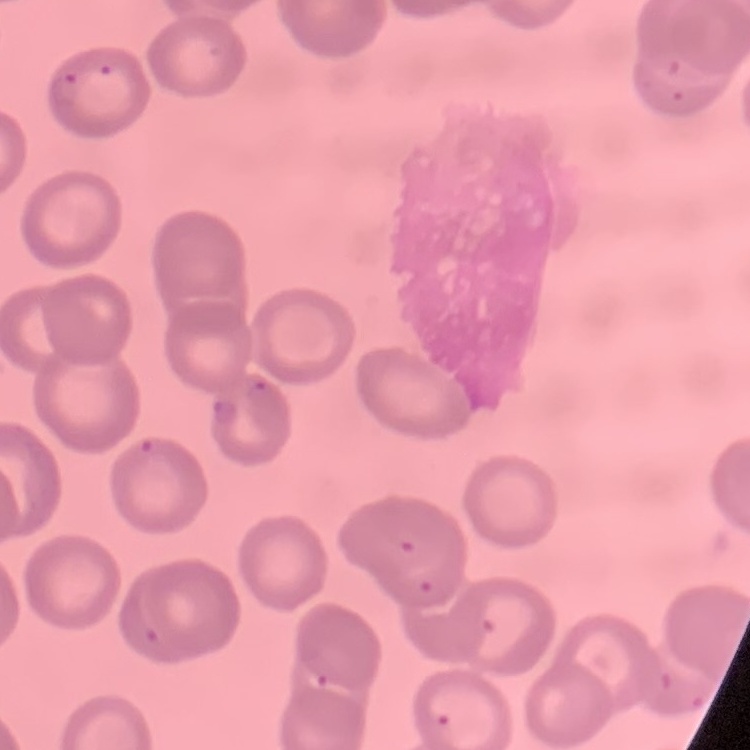

The erythrocytes exhibit no rouleaux formation. Thin blood smear. Stained with either Field's or Giemsa. Square crop of a larger photomicrograph.